State which cell type is depicted.
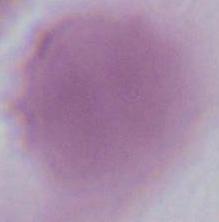
This is an erythrocyte.

Summary:
  - Magnification: 1000x
  - Modality: photomicrograph